Comment on the morphology of the red blood cells.
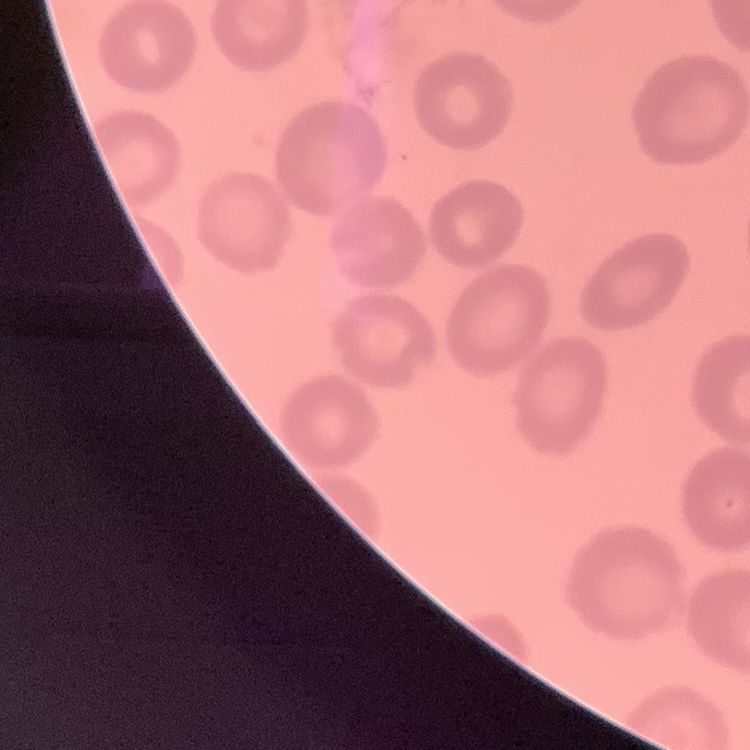

They show no rouleaux formation.

One tile cut from a larger photomicrograph. Stained with either Field's or Giemsa. Thin peripheral smear.